Outline each Plasmodium falciparum-infected red blood cell.
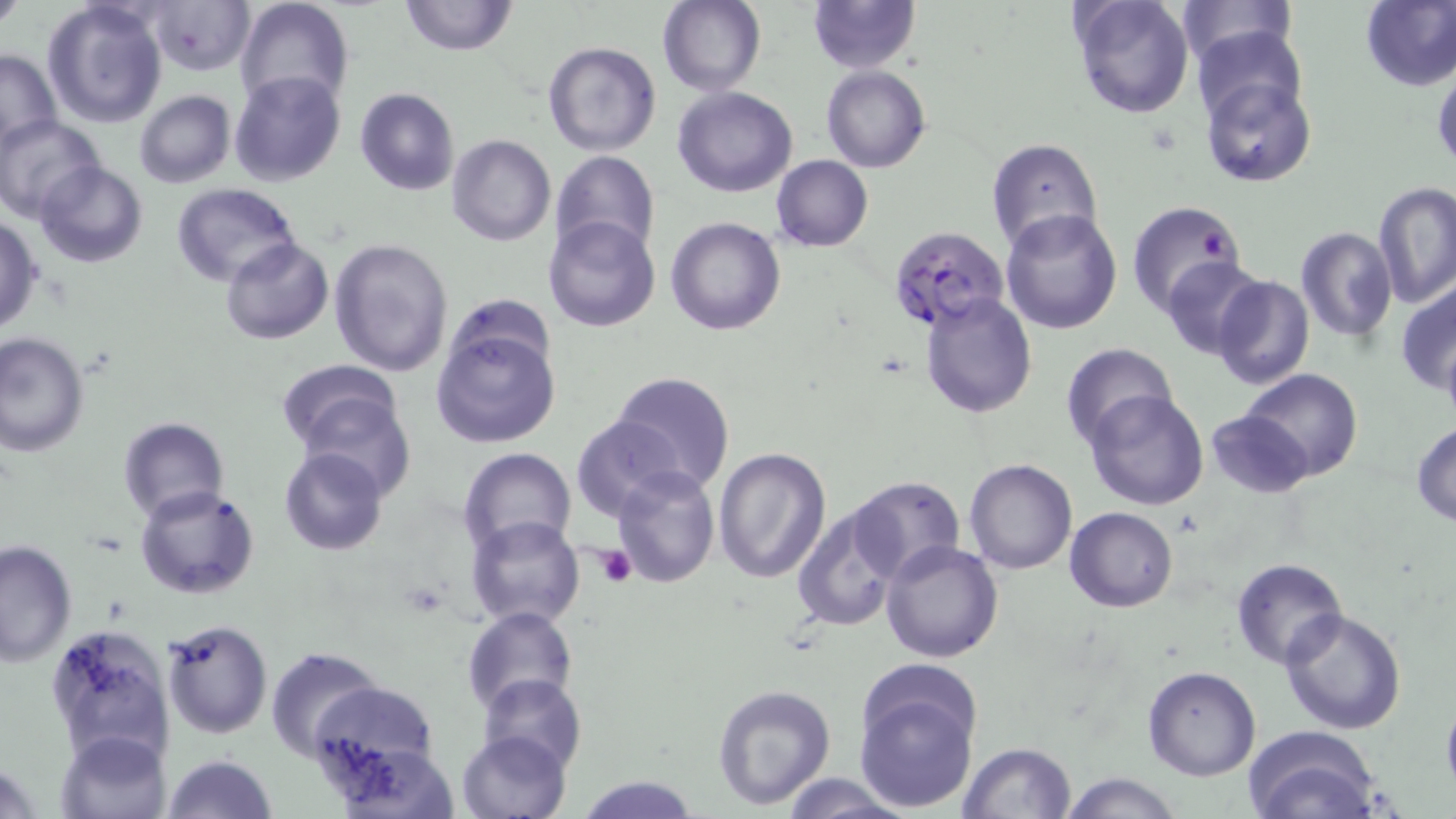
Approximate bounding boxes as [x1, y1, x2, y2] in pixels.
Plasmodium falciparum-infected red blood cells: [888, 224, 1010, 331].

Platelet locations: [594, 546, 637, 588]. Uninfected red blood cell locations: [0, 0, 26, 33], [42, 0, 167, 128], [235, 0, 355, 116], [400, 0, 517, 56], [806, 0, 921, 73], [1069, 0, 1196, 119], [1174, 0, 1296, 67], [1359, 0, 1456, 91], [657, 1, 766, 95], [144, 2, 253, 77], [1189, 23, 1308, 131], [542, 40, 661, 157], [1, 48, 62, 151], [1431, 65, 1456, 175], [822, 66, 929, 174], [229, 70, 345, 187], [1200, 76, 1316, 188], [672, 87, 798, 197], [355, 89, 459, 195], [134, 91, 235, 189], [0, 114, 103, 222], [447, 134, 556, 246], [985, 138, 1103, 253], [551, 150, 660, 264], [771, 155, 873, 252], [34, 159, 148, 268], [1373, 181, 1455, 310], [174, 183, 302, 287], [1125, 200, 1248, 316], [1001, 208, 1125, 334], [0, 215, 43, 335], [543, 215, 663, 333], [665, 218, 785, 336], [1296, 226, 1398, 343], [221, 236, 334, 345], [328, 240, 453, 377], [1161, 256, 1267, 359], [1211, 274, 1314, 391], [1396, 280, 1456, 402], [920, 292, 1037, 417], [431, 321, 562, 449], [0, 332, 89, 460], [1061, 344, 1181, 449], [276, 359, 411, 482], [1238, 367, 1364, 483], [608, 371, 734, 496], [1085, 388, 1212, 511], [1206, 409, 1315, 499], [116, 416, 229, 523], [570, 416, 680, 522], [1411, 421, 1456, 526], [279, 446, 387, 556], [713, 446, 833, 582], [458, 448, 577, 559], [963, 458, 1078, 576], [611, 467, 719, 587], [848, 475, 964, 585], [136, 485, 258, 600], [792, 501, 904, 633], [1067, 507, 1178, 612], [466, 516, 586, 629], [0, 539, 78, 667], [879, 540, 1003, 664], [1231, 560, 1347, 669], [462, 606, 578, 715], [1278, 607, 1407, 735], [162, 618, 273, 738], [44, 623, 175, 766], [265, 647, 383, 758], [1143, 666, 1261, 781], [853, 671, 985, 812], [479, 673, 585, 774], [307, 681, 440, 782], [712, 683, 836, 808], [1242, 726, 1382, 819], [457, 730, 570, 819], [57, 732, 171, 818], [957, 742, 1077, 819], [161, 755, 277, 819], [1056, 772, 1182, 818], [572, 775, 703, 817], [781, 775, 916, 818]. Slide-level diagnosis: Plasmodium falciparum. One field of a larger specimen. Image is 1456×819 pixels. Light microscopy. Thin blood film. May-Grünwald-Giemsa-stained preparation. Captured at 1000x magnification.